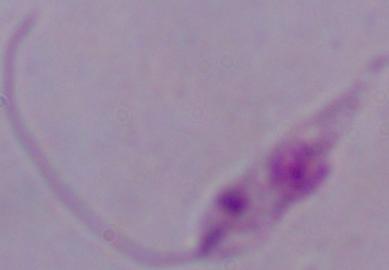
modality = micrograph
identification = Leishmania
magnification = 1000x